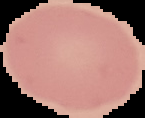
Image is 145×118 pixels. Result: negative for malaria parasites. From a thin blood smear. The area outside the segmented cell region is set to black.